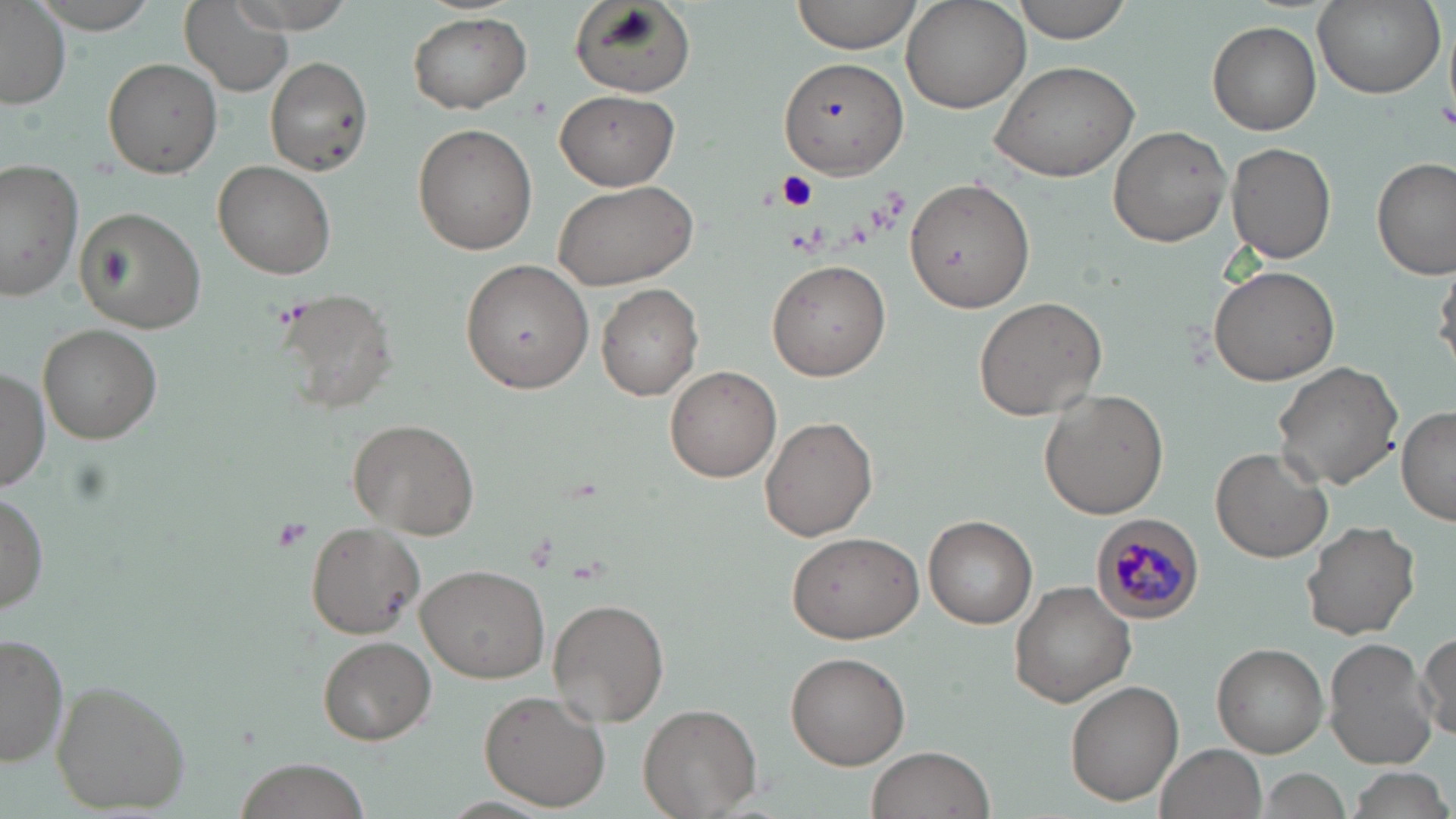

slide-level diagnosis = Plasmodium malariae
modality = light microscopy
magnification = 1000x
uninfected red blood cell locations = approximate bounding boxes as (x1, y1, x2, y2) in pixels: (24, 0, 166, 33), (216, 0, 366, 31), (788, 0, 919, 54), (1010, 0, 1133, 43), (569, 1, 694, 99), (900, 1, 1033, 114), (1312, 1, 1443, 97), (178, 3, 294, 96), (0, 4, 70, 108), (407, 13, 533, 113), (1209, 22, 1322, 134), (263, 55, 373, 176), (778, 56, 910, 179), (103, 58, 221, 177), (988, 60, 1140, 182), (556, 90, 677, 190), (412, 124, 538, 255), (1107, 125, 1232, 247), (1225, 143, 1335, 263), (1372, 157, 1455, 280), (213, 161, 337, 278), (0, 163, 81, 305), (552, 176, 700, 291), (906, 177, 1033, 313), (76, 206, 206, 333), (460, 257, 595, 394), (767, 259, 891, 381), (1208, 265, 1342, 387), (1433, 265, 1456, 373), (596, 283, 703, 400), (275, 286, 399, 412), (973, 296, 1108, 421), (39, 324, 162, 444), (1273, 360, 1402, 489), (665, 365, 781, 482), (0, 369, 49, 490), (1039, 390, 1168, 519), (1396, 407, 1455, 525), (759, 415, 878, 541), (347, 418, 479, 540), (1211, 447, 1332, 562), (0, 490, 48, 613), (923, 514, 1038, 628), (1301, 519, 1422, 640), (304, 520, 429, 640), (786, 531, 924, 643), (414, 564, 551, 681), (1009, 581, 1135, 707), (547, 598, 670, 726), (1414, 629, 1455, 741), (0, 632, 71, 770), (316, 635, 436, 745), (1323, 638, 1436, 769), (1212, 643, 1328, 757), (784, 651, 910, 769), (1064, 679, 1185, 806), (50, 680, 189, 812), (478, 689, 611, 810), (638, 703, 760, 817), (1157, 744, 1265, 819), (868, 747, 993, 818), (235, 758, 374, 819), (1340, 766, 1455, 819), (1252, 768, 1352, 819)
Plasmodium malariae-infected red blood cell locations = approximate bounding boxes as (x1, y1, x2, y2) in pixels: (1091, 514, 1204, 622)
preparation = thin blood film
image size = 1456×819 pixels
field of view = one of a larger specimen
stain = May-Grünwald-Giemsa
platelet locations = approximate bounding boxes as (x1, y1, x2, y2) in pixels: (1435, 96, 1456, 130), (776, 173, 821, 212), (269, 517, 313, 555)